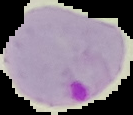

preparation = thin blood film
image size = 133×115 pixels
image type = segmented cell region with the area outside set to black
malaria status = parasitized